Assess the morphology of the erythrocytes.
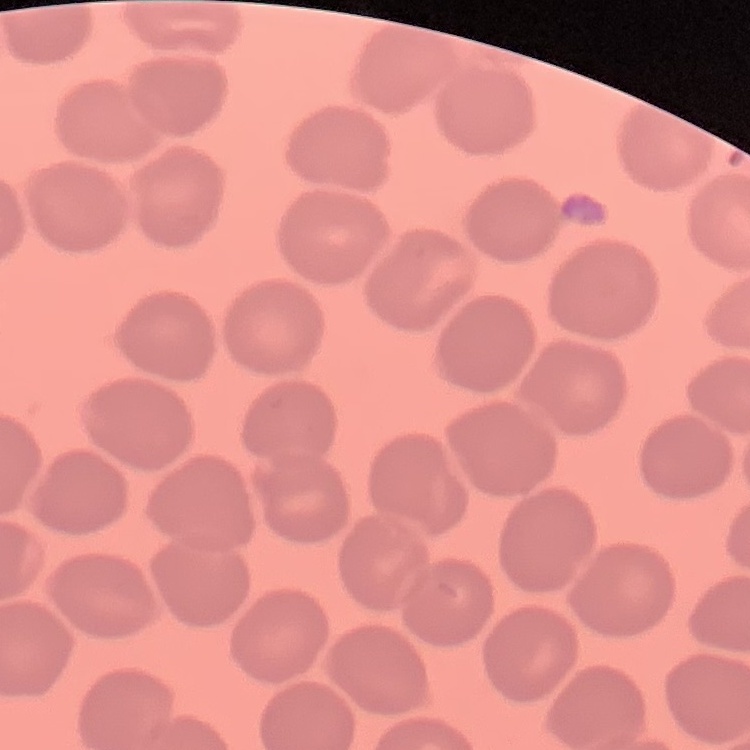

They show no rouleaux formation.

Square crop of a larger photomicrograph. Stained with either Field's or Giemsa. Thin blood film.